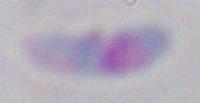 Photomicrograph. 1000x magnification. Toxoplasma gondii is shown.